Report the malaria status of this cell.
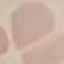

Uninfected.

Summary:
  - Preparation: thin blood smear
  - Stain: Giemsa
  - Capture: smartphone through the microscope eyepiece
  - Image type: cell patch, automatically extracted from a larger field of view and resized to 64 × 64 pixels